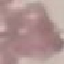
Summary:
  - Result: negative for malaria parasites
  - Preparation: thin blood film
  - Image type: automatically extracted cell patch, resized to 64 × 64 pixels
  - Stain: Giemsa
  - Capture: smartphone through the microscope eyepiece